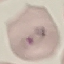
Summary:
  - Malaria status: parasitized
  - Capture: smartphone through the microscope eyepiece
  - Image type: cell patch, automatically extracted from a larger field of view and resized to 64 × 64 pixels
  - Preparation: thin blood film
  - Stain: Giemsa